Identify the parasite.
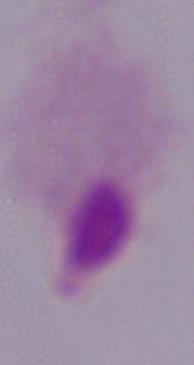
A trichomonad.

{
  "modality": "micrograph",
  "magnification": "1000x"
}